Locate and identify every blood parasite.
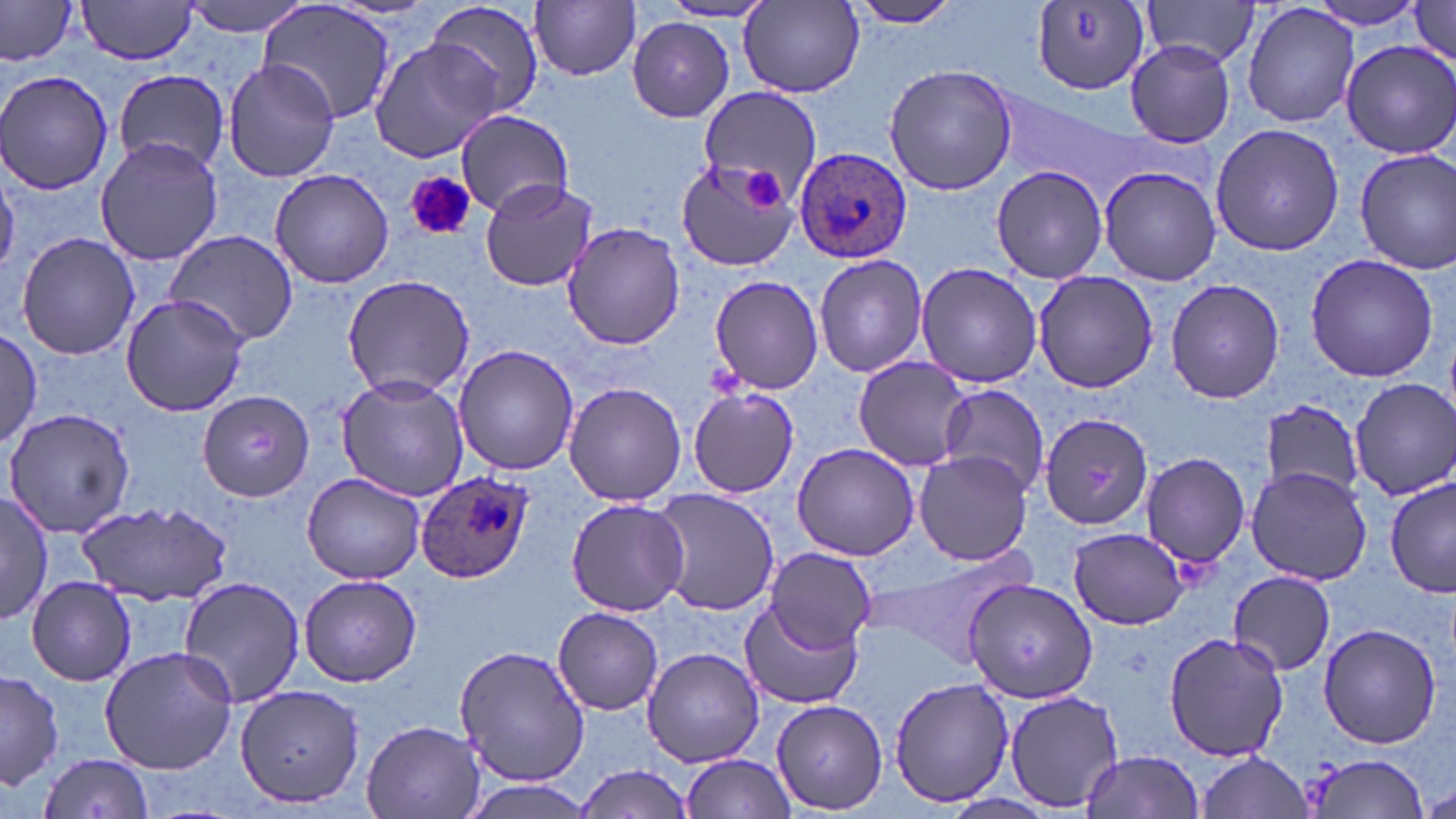

Approximate bounding boxes as named x1/y1/x2/y2 corners in pixels.
Plasmodium ovale-infected red blood cells: (x1=793, y1=148, x2=912, y2=266), (x1=417, y1=471, x2=533, y2=583).
No Plasmodium falciparum, Plasmodium malariae, Plasmodium vivax, Babesia divergens, or Trypanosoma brucei observed.

Platelet locations: (x1=743, y1=169, x2=785, y2=211), (x1=404, y1=170, x2=476, y2=241). Uninfected red blood cell locations: (x1=75, y1=0, x2=201, y2=65), (x1=182, y1=0, x2=316, y2=38), (x1=843, y1=0, x2=963, y2=27), (x1=1142, y1=0, x2=1266, y2=72), (x1=1302, y1=0, x2=1434, y2=31), (x1=423, y1=1, x2=546, y2=118), (x1=531, y1=1, x2=642, y2=81), (x1=1407, y1=1, x2=1455, y2=66), (x1=1029, y1=2, x2=1151, y2=94), (x1=1241, y1=2, x2=1359, y2=127), (x1=0, y1=3, x2=76, y2=67), (x1=256, y1=3, x2=397, y2=125), (x1=659, y1=3, x2=774, y2=23), (x1=739, y1=3, x2=866, y2=98), (x1=626, y1=18, x2=735, y2=122), (x1=368, y1=40, x2=504, y2=163), (x1=1123, y1=40, x2=1238, y2=149), (x1=1340, y1=40, x2=1456, y2=162), (x1=223, y1=59, x2=339, y2=183), (x1=884, y1=64, x2=1019, y2=195), (x1=0, y1=70, x2=119, y2=193), (x1=115, y1=70, x2=228, y2=173), (x1=697, y1=85, x2=821, y2=202), (x1=994, y1=87, x2=1133, y2=196), (x1=455, y1=109, x2=575, y2=217), (x1=1210, y1=123, x2=1348, y2=257), (x1=94, y1=135, x2=222, y2=265), (x1=1355, y1=148, x2=1456, y2=275), (x1=675, y1=155, x2=803, y2=274), (x1=0, y1=159, x2=22, y2=273), (x1=989, y1=165, x2=1108, y2=282), (x1=1096, y1=166, x2=1222, y2=285), (x1=269, y1=168, x2=394, y2=288), (x1=479, y1=177, x2=599, y2=294), (x1=561, y1=224, x2=688, y2=350), (x1=165, y1=229, x2=298, y2=347), (x1=16, y1=232, x2=141, y2=360), (x1=813, y1=253, x2=928, y2=378), (x1=1304, y1=253, x2=1439, y2=383), (x1=915, y1=261, x2=1043, y2=388), (x1=1031, y1=270, x2=1160, y2=392), (x1=341, y1=274, x2=475, y2=398), (x1=709, y1=276, x2=825, y2=394), (x1=1166, y1=278, x2=1285, y2=404), (x1=119, y1=294, x2=250, y2=417), (x1=1, y1=328, x2=42, y2=448), (x1=452, y1=344, x2=581, y2=475), (x1=851, y1=355, x2=973, y2=473), (x1=337, y1=376, x2=468, y2=500), (x1=1350, y1=379, x2=1456, y2=498), (x1=563, y1=382, x2=687, y2=507), (x1=935, y1=383, x2=1049, y2=494), (x1=686, y1=387, x2=799, y2=497), (x1=196, y1=391, x2=317, y2=502), (x1=1259, y1=400, x2=1367, y2=498), (x1=4, y1=406, x2=136, y2=537), (x1=1039, y1=412, x2=1155, y2=532), (x1=792, y1=443, x2=919, y2=561), (x1=913, y1=449, x2=1033, y2=565), (x1=1139, y1=453, x2=1249, y2=570), (x1=1246, y1=465, x2=1373, y2=586), (x1=302, y1=472, x2=427, y2=584), (x1=1385, y1=477, x2=1455, y2=599), (x1=651, y1=489, x2=779, y2=617), (x1=0, y1=492, x2=51, y2=627), (x1=564, y1=497, x2=691, y2=617), (x1=79, y1=501, x2=233, y2=602), (x1=1067, y1=526, x2=1192, y2=630), (x1=763, y1=545, x2=877, y2=655), (x1=1228, y1=570, x2=1337, y2=676), (x1=298, y1=573, x2=422, y2=687), (x1=25, y1=576, x2=136, y2=686), (x1=175, y1=576, x2=307, y2=708), (x1=964, y1=577, x2=1099, y2=705), (x1=739, y1=600, x2=862, y2=710), (x1=553, y1=607, x2=664, y2=715), (x1=1318, y1=623, x2=1442, y2=749), (x1=1162, y1=629, x2=1287, y2=763), (x1=454, y1=643, x2=591, y2=787), (x1=99, y1=645, x2=238, y2=775), (x1=641, y1=646, x2=766, y2=768), (x1=0, y1=669, x2=64, y2=790), (x1=889, y1=676, x2=1014, y2=808), (x1=235, y1=682, x2=367, y2=808), (x1=1005, y1=689, x2=1125, y2=812), (x1=771, y1=698, x2=887, y2=813), (x1=360, y1=719, x2=486, y2=819), (x1=1080, y1=750, x2=1207, y2=818), (x1=1195, y1=750, x2=1313, y2=818), (x1=680, y1=753, x2=797, y2=818), (x1=35, y1=754, x2=157, y2=819), (x1=1304, y1=754, x2=1432, y2=817), (x1=575, y1=764, x2=695, y2=817), (x1=457, y1=778, x2=599, y2=819), (x1=1424, y1=784, x2=1456, y2=817). Slide-level diagnosis: Plasmodium ovale. One field of a larger specimen. May-Grünwald-Giemsa stain. Captured at 1000x magnification. Thin blood smear. Optical microscopy. Image is 1456×819 pixels.